State which cell type is depicted.
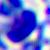
This is a leukocyte.

Summary:
  - Modality: photomicrograph
  - Magnification: 400x